Describe the morphology of the red blood cells.
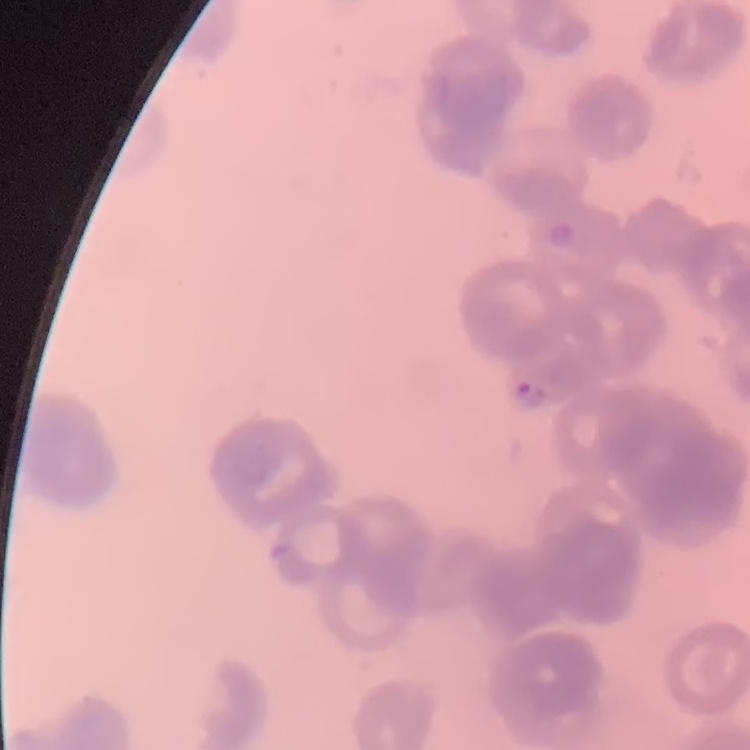
Rouleaux formation.

stain: Field's or Giemsa
preparation: thin peripheral smear
image_type: square crop of a larger photomicrograph